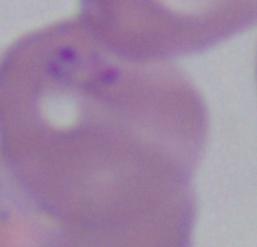

magnification = 1000x
modality = micrograph
identification = Babesia